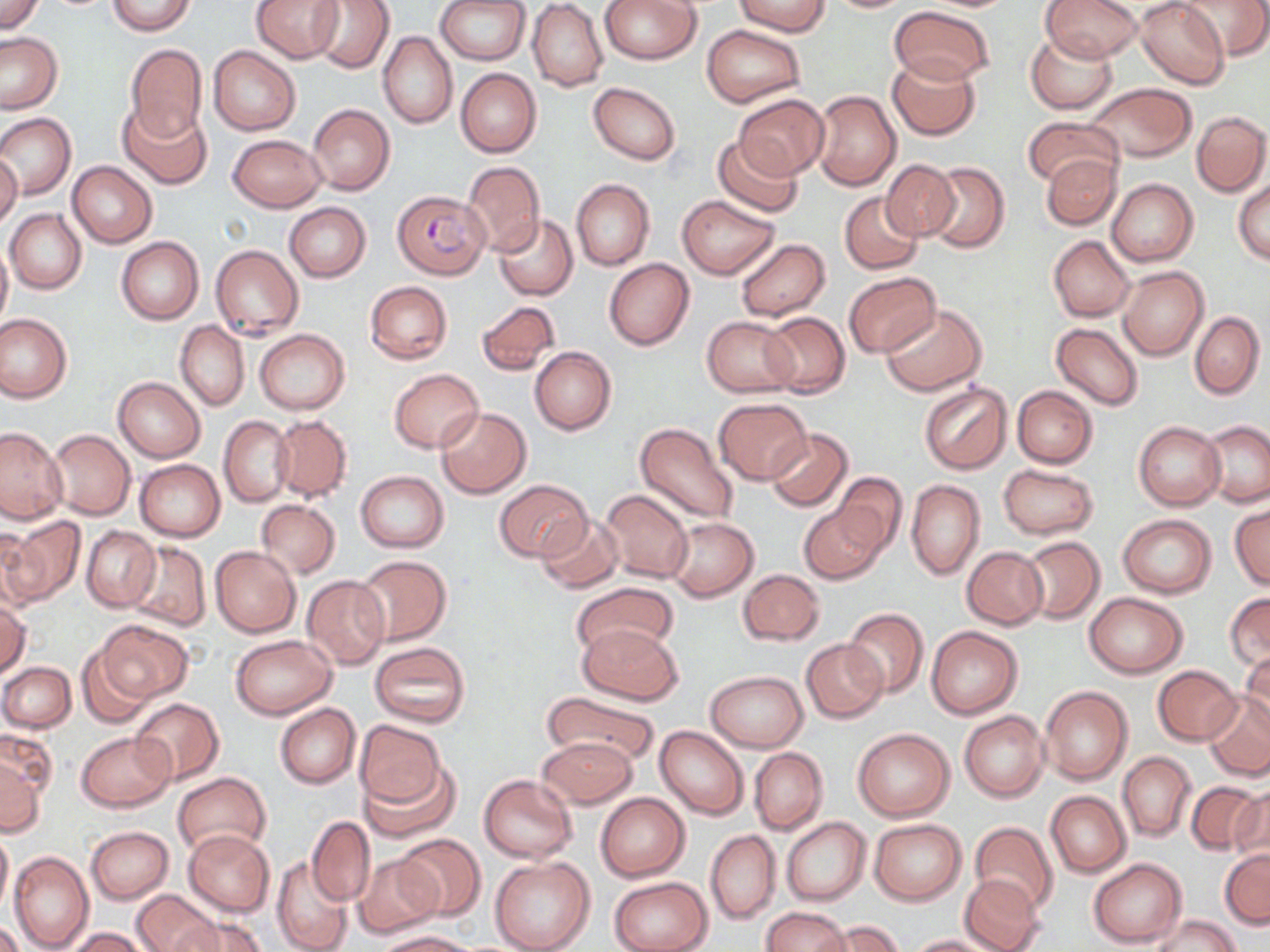

Summary:
  - Coordinate format: approximate bounding boxes as [x1, y1, x2, y2] in pixels
  - Uninfected red blood cell locations: [0, 0, 45, 35], [252, 0, 345, 63], [312, 0, 394, 73], [436, 0, 529, 65], [600, 0, 702, 65], [1041, 0, 1141, 61], [1136, 0, 1228, 89], [1180, 0, 1270, 61], [106, 1, 196, 35], [733, 1, 829, 36], [821, 1, 917, 13], [527, 2, 607, 91], [530, 4, 691, 79], [890, 6, 997, 87], [703, 25, 807, 108], [0, 31, 64, 114], [1024, 31, 1118, 113], [379, 33, 457, 129], [124, 44, 206, 143], [208, 45, 301, 136], [886, 53, 981, 140], [455, 68, 542, 158], [588, 82, 681, 165], [1083, 84, 1196, 163], [810, 89, 901, 191], [734, 92, 829, 181], [119, 101, 212, 189], [308, 104, 395, 195], [1192, 111, 1269, 195], [1, 113, 76, 199], [1021, 116, 1122, 190], [228, 134, 326, 211], [712, 135, 805, 217], [0, 148, 22, 232], [1041, 153, 1121, 231], [67, 161, 157, 248], [882, 161, 961, 241], [462, 162, 545, 255], [924, 162, 1009, 253], [1106, 178, 1198, 266], [571, 179, 654, 269], [1233, 179, 1270, 265], [839, 192, 924, 274], [677, 194, 780, 279], [284, 202, 371, 282], [5, 209, 87, 294], [493, 215, 578, 301], [1047, 235, 1136, 321], [0, 237, 11, 333], [117, 237, 203, 325], [735, 238, 830, 321], [211, 244, 304, 341], [604, 258, 694, 350], [1117, 266, 1208, 361], [844, 272, 940, 359], [365, 281, 453, 363], [477, 300, 562, 376], [881, 303, 986, 396], [1189, 310, 1264, 399], [761, 311, 850, 397], [0, 313, 71, 402], [701, 316, 798, 397], [176, 321, 250, 411], [1050, 322, 1142, 410], [254, 329, 350, 414], [530, 347, 617, 435], [388, 369, 484, 452], [113, 376, 205, 462], [919, 381, 1012, 474], [1012, 385, 1097, 468], [714, 398, 810, 484], [435, 406, 531, 499], [270, 415, 352, 500], [219, 417, 294, 507], [1200, 420, 1270, 507], [1134, 422, 1224, 510], [634, 423, 740, 526], [0, 427, 67, 522], [45, 429, 136, 520], [765, 429, 854, 511], [134, 459, 225, 541], [997, 464, 1100, 540], [355, 471, 448, 551], [830, 472, 907, 556], [493, 478, 592, 563], [906, 479, 984, 580], [599, 490, 694, 582], [256, 500, 341, 577], [1229, 501, 1269, 591], [799, 502, 887, 584], [534, 514, 624, 593], [1118, 514, 1218, 598], [667, 516, 758, 600], [2, 518, 85, 608], [0, 526, 38, 615], [81, 526, 160, 612], [1020, 535, 1105, 624], [126, 540, 210, 631], [211, 546, 301, 637], [962, 546, 1048, 629], [354, 555, 451, 645], [738, 568, 824, 645], [302, 575, 391, 669], [573, 582, 680, 661], [1083, 592, 1188, 678], [0, 593, 29, 681], [1225, 593, 1270, 673], [845, 609, 928, 698], [98, 620, 192, 702], [577, 623, 684, 705], [925, 625, 1023, 720], [230, 635, 337, 719], [801, 638, 888, 722], [370, 642, 471, 729], [75, 647, 158, 728], [1239, 650, 1269, 736], [0, 661, 75, 731], [1152, 664, 1242, 744], [706, 670, 807, 751], [1039, 685, 1132, 785], [540, 690, 660, 771], [1204, 694, 1270, 781], [132, 698, 223, 784], [275, 704, 360, 787], [959, 710, 1049, 803], [354, 720, 447, 812], [656, 725, 748, 820], [0, 727, 55, 805], [852, 727, 955, 821], [76, 730, 175, 812], [536, 736, 636, 810], [750, 747, 828, 835], [1118, 752, 1195, 841], [0, 756, 45, 838], [360, 760, 459, 842], [172, 771, 271, 857], [479, 774, 577, 862], [1185, 781, 1267, 856], [1230, 785, 1270, 867], [596, 791, 690, 881], [1046, 791, 1131, 876], [307, 817, 376, 906], [781, 817, 871, 906], [869, 819, 966, 904], [970, 822, 1059, 916], [288, 824, 396, 938], [86, 826, 173, 905], [0, 827, 12, 916], [182, 827, 274, 916], [705, 830, 780, 924], [395, 834, 485, 922], [1219, 849, 1269, 928], [9, 850, 93, 952], [354, 854, 443, 939], [489, 856, 595, 952], [1088, 857, 1187, 948], [272, 858, 353, 952], [959, 874, 1045, 952], [608, 876, 713, 952], [133, 889, 218, 952], [760, 906, 851, 952], [175, 914, 268, 952], [1153, 914, 1238, 952], [820, 920, 904, 952], [0, 922, 24, 952], [67, 927, 147, 951], [374, 931, 478, 952], [907, 934, 1003, 952]
  - Plasmodium falciparum-infected red blood cell locations: [392, 190, 489, 280]
  - Slide-level diagnosis: Plasmodium falciparum
  - Image size: 1270×952 pixels
  - Magnification: 1000x
  - Preparation: thin blood film
  - Modality: light microscopy
  - Field of view: single
  - Stain: May-Grünwald-Giemsa